Report the malaria status of this cell.
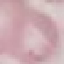
It is uninfected.

Summary:
  - Capture: smartphone through the microscope eyepiece
  - Stain: Giemsa
  - Preparation: thin blood film
  - Image type: automatically extracted cell patch, resized to 64 × 64 pixels